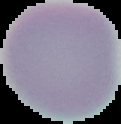
image type = cell region segmented out of the field of view; surrounding area masked to black
image size = 121×124 pixels
preparation = thin blood film
malaria status = uninfected